Give a bounding box for every leukocyte visible.
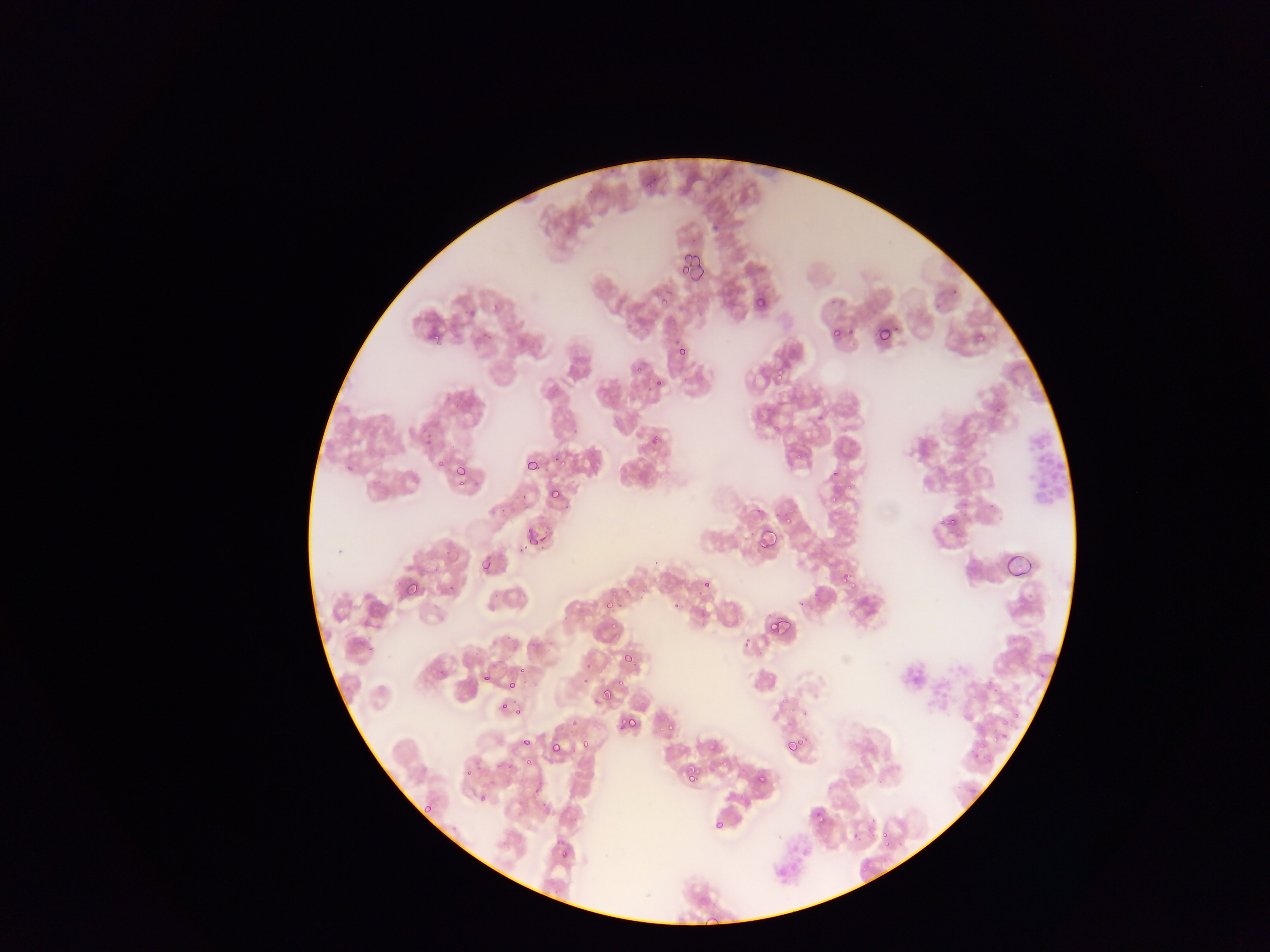
No leukocytes observed.

plasmodium_parasite_locations: 'approximate bounding boxes as {left, top, right, bottom} in pixels: {645, 180, 653, 188}, {677, 251, 703, 278}, {677, 252, 693, 271}, {656, 293, 668, 306}, {755, 298, 766, 308}, {875, 324, 892, 343}, {830, 327, 841, 338}, {431, 332, 441, 342}, {975, 332, 986, 342}, {676, 347, 687, 359}, {776, 364, 789, 377}, {653, 377, 663, 387}, {434, 452, 446, 470}, {548, 454, 567, 469}, {525, 458, 540, 471}, {454, 463, 468, 478}, {549, 488, 560, 498}, {825, 489, 838, 510}, {781, 512, 793, 525}, {944, 514, 958, 527}, {517, 524, 551, 549}, {758, 528, 776, 548}, {481, 560, 492, 572}, {840, 571, 853, 585}, {401, 579, 420, 597}, {701, 580, 710, 588}, {443, 583, 456, 594}, {601, 600, 613, 612}, {673, 603, 682, 612}, {767, 618, 785, 634}, {611, 621, 620, 632}, {740, 637, 752, 653}, {625, 654, 638, 668}, {517, 667, 526, 676}, {483, 672, 493, 681}, {482, 673, 490, 682}, {506, 678, 518, 691}, {593, 684, 615, 701}, {497, 702, 509, 721}, {514, 706, 524, 715}, {990, 706, 1015, 749}, {629, 708, 643, 729}, {663, 720, 675, 732}, {607, 724, 618, 736}, {786, 737, 804, 753}, {521, 738, 531, 747}, {703, 740, 717, 753}, {784, 740, 798, 752}, {579, 741, 588, 751}, {550, 743, 562, 754}, {522, 754, 530, 767}, {502, 755, 518, 774}, {684, 768, 697, 781}, {463, 769, 472, 779}, {755, 774, 766, 785}, {530, 782, 542, 799}, {479, 792, 487, 802}, {813, 809, 824, 819}, {712, 818, 724, 830}, {880, 830, 889, 842}, {553, 844, 572, 858}'
image_size: 1270×952 pixels
country: Ghana
field_of_view: single
preparation: thin blood film
capture: mobile-phone photograph through a microscope